Name the blood parasite species.
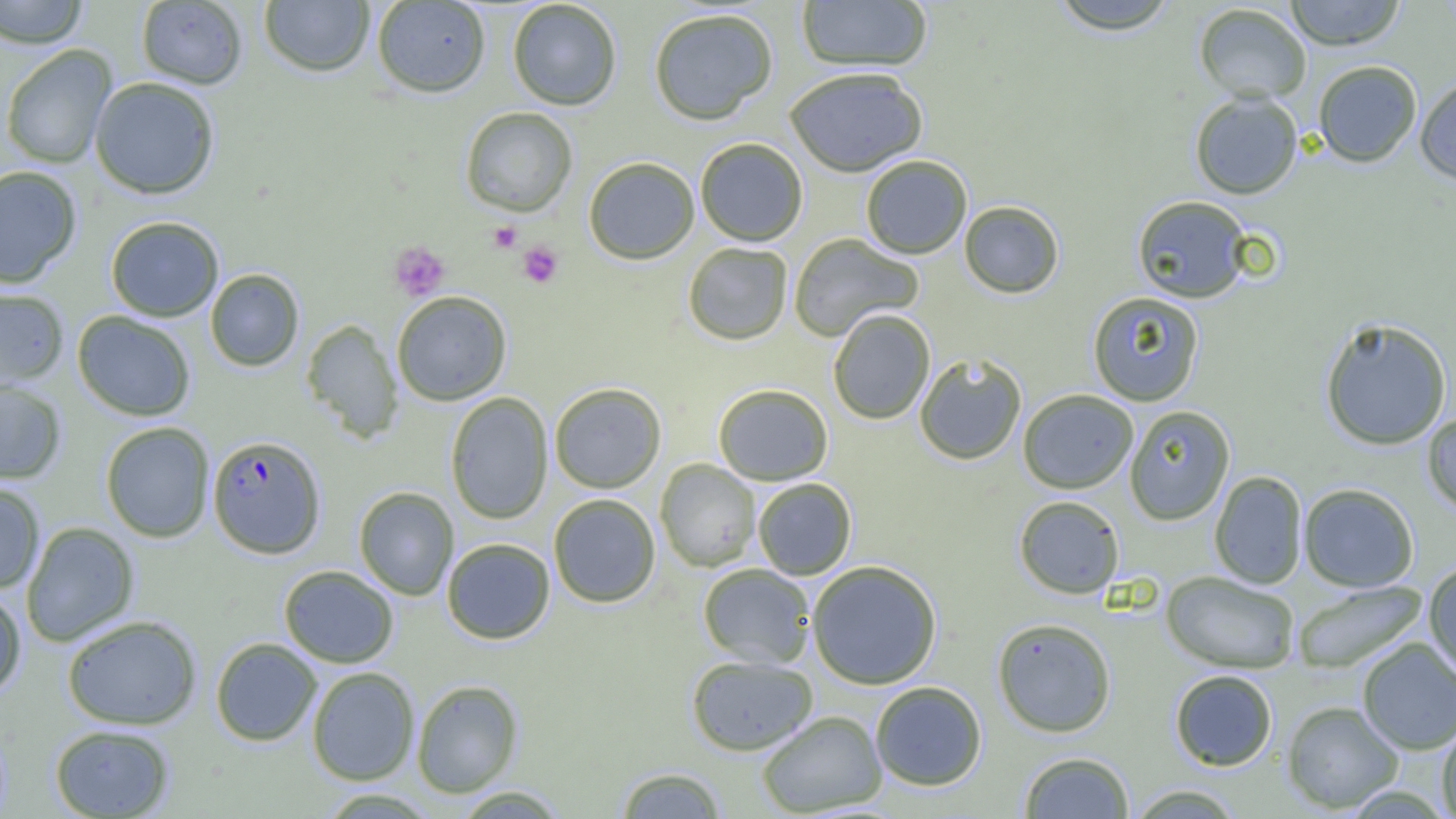
Plasmodium falciparum.

Summary:
  - Coordinate format: approximate bounding boxes as [x1, y1, x2, y2] in pixels
  - Plasmodium falciparum-infected red blood cell locations: [207, 435, 326, 558]
  - Uninfected red blood cell locations: [0, 0, 90, 49], [796, 0, 932, 72], [1046, 0, 1183, 35], [1283, 0, 1406, 50], [136, 1, 248, 89], [258, 1, 375, 77], [371, 1, 491, 98], [507, 1, 622, 110], [1193, 3, 1312, 103], [648, 7, 778, 125], [0, 45, 117, 169], [1312, 60, 1422, 167], [784, 67, 928, 177], [1414, 76, 1456, 184], [89, 77, 220, 199], [1189, 91, 1303, 199], [460, 107, 578, 217], [695, 138, 808, 246], [861, 155, 972, 259], [583, 157, 700, 265], [0, 165, 82, 288], [1131, 194, 1254, 304], [959, 201, 1064, 298], [105, 216, 224, 321], [788, 233, 923, 341], [682, 242, 793, 345], [205, 268, 304, 371], [0, 287, 69, 389], [391, 291, 512, 406], [1087, 291, 1205, 406], [828, 309, 935, 425], [72, 311, 196, 421], [1319, 317, 1452, 450], [301, 319, 404, 443], [914, 353, 1027, 466], [0, 379, 67, 485], [549, 382, 667, 493], [713, 383, 833, 485], [1017, 389, 1138, 494], [445, 392, 553, 525], [1124, 405, 1235, 525], [1422, 412, 1456, 516], [100, 422, 215, 542], [655, 459, 760, 572], [1209, 471, 1308, 589], [752, 478, 857, 580], [0, 482, 46, 593], [1298, 483, 1419, 592], [353, 486, 459, 600], [548, 494, 660, 608], [1013, 495, 1125, 599], [21, 522, 139, 647], [441, 538, 555, 644], [806, 560, 943, 689], [1422, 560, 1456, 681], [697, 563, 816, 668], [278, 565, 399, 668], [1161, 571, 1300, 674], [1292, 581, 1427, 674], [0, 587, 26, 701], [62, 614, 202, 730], [992, 618, 1117, 737], [210, 637, 322, 746], [1357, 638, 1456, 755], [685, 654, 818, 756], [306, 666, 420, 785], [1169, 669, 1278, 771], [411, 679, 523, 797], [870, 681, 987, 791], [1281, 700, 1404, 813], [756, 710, 887, 816], [1436, 720, 1456, 818], [49, 724, 175, 818], [1018, 751, 1135, 818], [615, 766, 728, 818], [1126, 784, 1246, 818], [450, 785, 571, 818], [316, 789, 440, 819]
  - Platelet locations: [488, 222, 522, 253], [388, 241, 451, 301], [517, 241, 563, 288]
  - Preparation: thin blood smear
  - Image size: 1456×819 pixels
  - Field of view: single
  - Magnification: 1000x
  - Modality: light microscopy